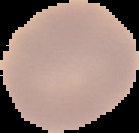 Cell region segmented out of the field of view; the surrounding area is masked to black. Result: no malaria parasites seen. Image is 139×133 pixels. From a thin blood film.